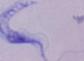
Summary:
  - Modality: micrograph
  - Identification: trypanosome
  - Magnification: 1000x